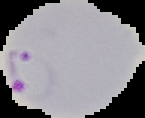

preparation = thin blood smear
image type = segmented cell region with the area outside set to black
result = Plasmodium parasites identified
image size = 145×118 pixels